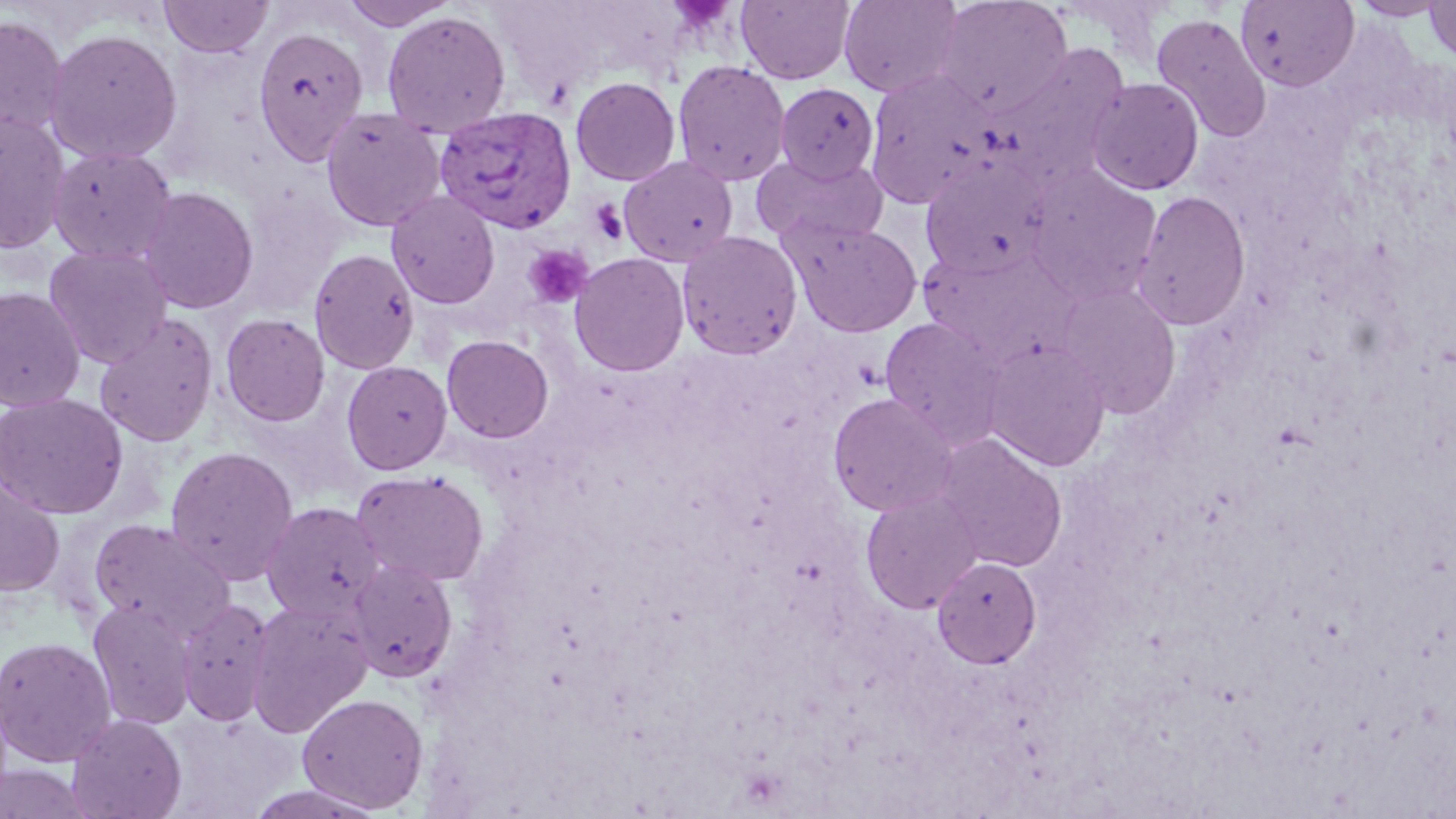
slide-level diagnosis = Plasmodium vivax
preparation = thin blood smear
platelet locations = approximate bounding boxes as named x1/y1/x2/y2 corners in pixels: (x1=590, y1=200, x2=629, y2=245), (x1=523, y1=245, x2=593, y2=309)
image size = 1456×819 pixels
magnification = 1000x
modality = light microscopy
field of view = single
stain = May-Grünwald-Giemsa
uninfected red blood cell locations = approximate bounding boxes as named x1/y1/x2/y2 corners in pixels: (x1=160, y1=0, x2=272, y2=58), (x1=340, y1=0, x2=459, y2=31), (x1=736, y1=0, x2=855, y2=84), (x1=838, y1=0, x2=964, y2=98), (x1=935, y1=0, x2=1074, y2=117), (x1=1348, y1=0, x2=1451, y2=20), (x1=1235, y1=1, x2=1360, y2=91), (x1=1423, y1=1, x2=1456, y2=65), (x1=382, y1=11, x2=511, y2=136), (x1=1151, y1=13, x2=1272, y2=143), (x1=0, y1=15, x2=68, y2=141), (x1=252, y1=25, x2=368, y2=165), (x1=44, y1=28, x2=182, y2=164), (x1=988, y1=42, x2=1131, y2=191), (x1=672, y1=61, x2=791, y2=186), (x1=863, y1=69, x2=999, y2=210), (x1=570, y1=76, x2=681, y2=186), (x1=1086, y1=78, x2=1204, y2=196), (x1=774, y1=83, x2=880, y2=183), (x1=320, y1=107, x2=446, y2=232), (x1=0, y1=112, x2=71, y2=256), (x1=47, y1=145, x2=177, y2=265), (x1=751, y1=152, x2=889, y2=249), (x1=619, y1=155, x2=738, y2=267), (x1=920, y1=158, x2=1055, y2=280), (x1=1023, y1=166, x2=1163, y2=304), (x1=136, y1=186, x2=259, y2=314), (x1=1131, y1=189, x2=1252, y2=331), (x1=386, y1=190, x2=500, y2=310), (x1=784, y1=217, x2=923, y2=337), (x1=677, y1=230, x2=803, y2=360), (x1=43, y1=245, x2=172, y2=368), (x1=917, y1=247, x2=1072, y2=364), (x1=308, y1=248, x2=420, y2=374), (x1=569, y1=252, x2=690, y2=376), (x1=1054, y1=282, x2=1182, y2=418), (x1=0, y1=287, x2=85, y2=412), (x1=94, y1=312, x2=219, y2=447), (x1=220, y1=313, x2=330, y2=426), (x1=879, y1=316, x2=1006, y2=446), (x1=441, y1=335, x2=554, y2=443), (x1=983, y1=338, x2=1111, y2=472), (x1=341, y1=360, x2=453, y2=475), (x1=0, y1=392, x2=128, y2=519), (x1=827, y1=392, x2=959, y2=516), (x1=934, y1=432, x2=1068, y2=573), (x1=165, y1=445, x2=300, y2=585), (x1=351, y1=469, x2=489, y2=587), (x1=0, y1=477, x2=65, y2=597), (x1=860, y1=487, x2=983, y2=614), (x1=260, y1=501, x2=385, y2=624), (x1=88, y1=518, x2=236, y2=640), (x1=932, y1=556, x2=1041, y2=669), (x1=346, y1=558, x2=459, y2=683), (x1=175, y1=598, x2=274, y2=727), (x1=87, y1=599, x2=198, y2=731), (x1=246, y1=600, x2=372, y2=737), (x1=25, y1=604, x2=162, y2=745), (x1=0, y1=636, x2=116, y2=767), (x1=296, y1=692, x2=429, y2=813), (x1=67, y1=713, x2=187, y2=819), (x1=0, y1=763, x2=93, y2=818), (x1=241, y1=783, x2=389, y2=818)
Plasmodium vivax-infected red blood cell locations = approximate bounding boxes as named x1/y1/x2/y2 corners in pixels: (x1=434, y1=106, x2=577, y2=233)